Locate every Plasmodium vivax-infected red blood cell.
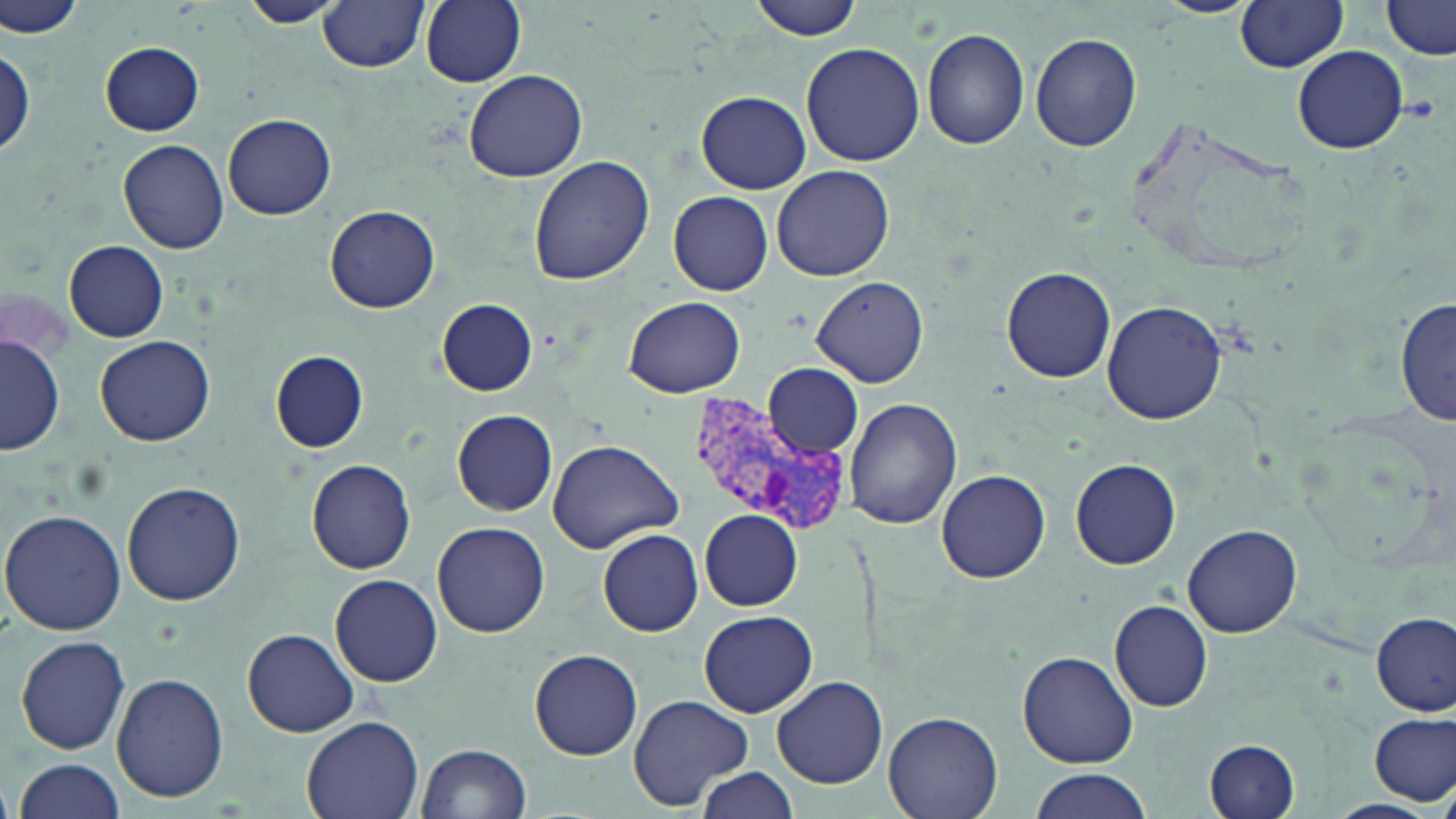
Approximate bounding boxes as (x1, y1, x2, y2) in pixels.
Plasmodium vivax-infected red blood cells: (690, 394, 853, 534).

{
  "slide_level_diagnosis": "Plasmodium vivax",
  "magnification": "1000x",
  "field_of_view": "single",
  "uninfected_red_blood_cell_locations": "approximate bounding boxes as (x1, y1, x2, y2) in pixels: (239, 0, 342, 27), (317, 0, 429, 72), (418, 0, 528, 88), (749, 0, 867, 41), (1382, 0, 1456, 58), (3, 1, 89, 41), (1234, 1, 1351, 72), (922, 28, 1030, 150), (1030, 32, 1143, 152), (99, 41, 206, 135), (800, 43, 927, 169), (0, 45, 34, 163), (1292, 45, 1409, 155), (462, 68, 588, 182), (696, 90, 810, 194), (224, 112, 337, 220), (118, 138, 229, 253), (528, 155, 653, 284), (771, 165, 893, 281), (668, 192, 773, 295), (325, 206, 440, 313), (64, 240, 168, 341), (1001, 266, 1117, 384), (811, 275, 928, 388), (625, 295, 747, 398), (1394, 297, 1454, 429), (437, 298, 537, 395), (1102, 300, 1229, 425), (95, 335, 216, 446), (3, 336, 65, 455), (270, 351, 367, 452), (761, 364, 864, 457), (845, 398, 962, 529), (453, 410, 556, 515), (548, 438, 683, 551), (306, 459, 416, 574), (1070, 459, 1181, 570), (936, 469, 1051, 584), (121, 481, 247, 607), (0, 507, 129, 634), (700, 510, 803, 611), (432, 522, 550, 638), (1181, 524, 1303, 638), (597, 529, 703, 636), (331, 574, 442, 687), (1109, 600, 1212, 711), (698, 610, 818, 718), (1372, 612, 1455, 716), (243, 628, 360, 736), (15, 633, 131, 754), (528, 648, 643, 760), (1018, 650, 1139, 768), (112, 672, 229, 802), (772, 676, 888, 789), (626, 694, 755, 810), (1371, 711, 1455, 805), (882, 712, 1003, 819), (300, 715, 424, 819), (1205, 738, 1300, 819), (416, 743, 531, 819), (14, 756, 128, 819), (692, 765, 798, 819), (1029, 769, 1151, 819)",
  "modality": "optical microscopy",
  "image_size": "1456×819 pixels",
  "preparation": "thin blood film",
  "stain": "May-Grünwald-Giemsa"
}